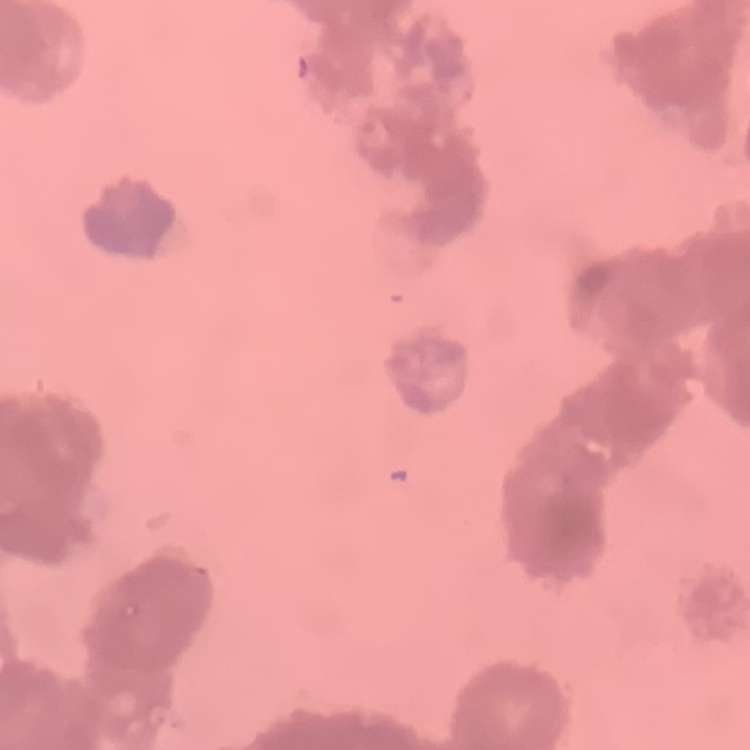

The erythrocytes show rouleaux formation. Square crop of a larger photomicrograph. Thin blood smear. Field's or Giemsa stain.